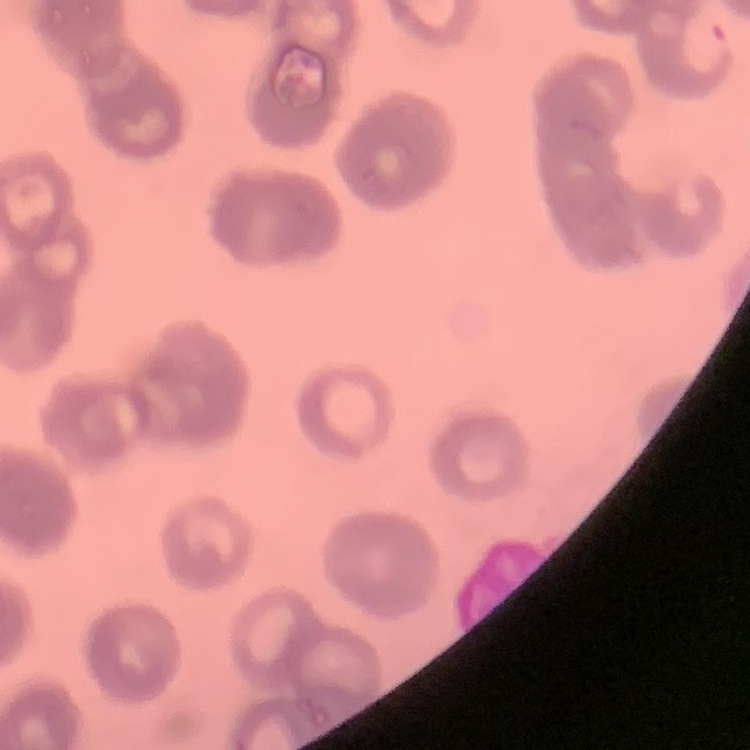

The red blood cells exhibit rouleaux formation. One tile cut from a larger photomicrograph. Thin blood film. Field's or Giemsa stain.